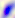
magnification: 400x
identification: Toxoplasma gondii
modality: photomicrograph